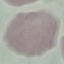 Malaria status: uninfected. Giemsa-stained preparation. Thin smear of blood. Automatically extracted cell patch, resized to 64 × 64 pixels. Acquired by smartphone through the microscope eyepiece.